Comment on the morphology of the erythrocytes.
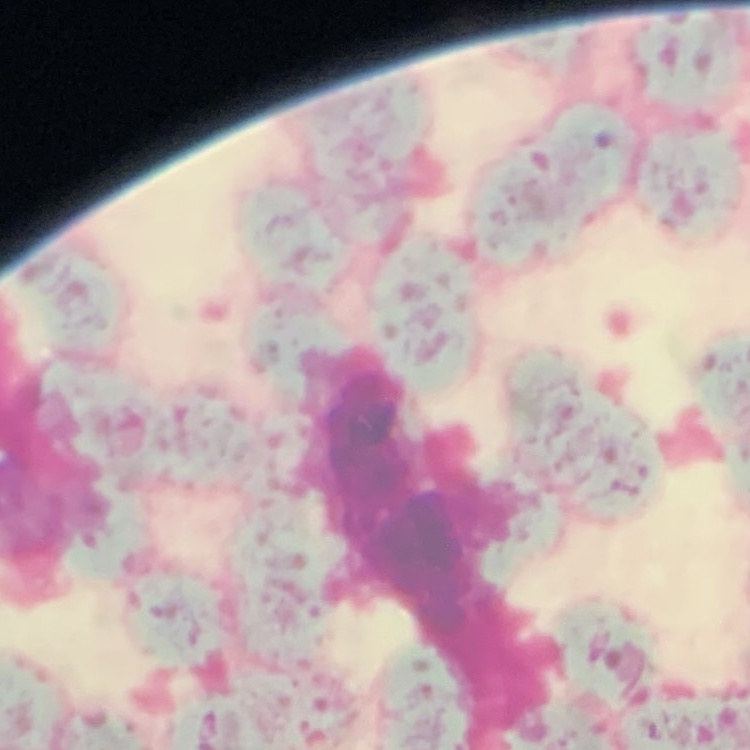

Rouleaux formation.

image type = square crop of a larger photomicrograph
preparation = thin peripheral smear
stain = Field's or Giemsa